Give the preparation type.
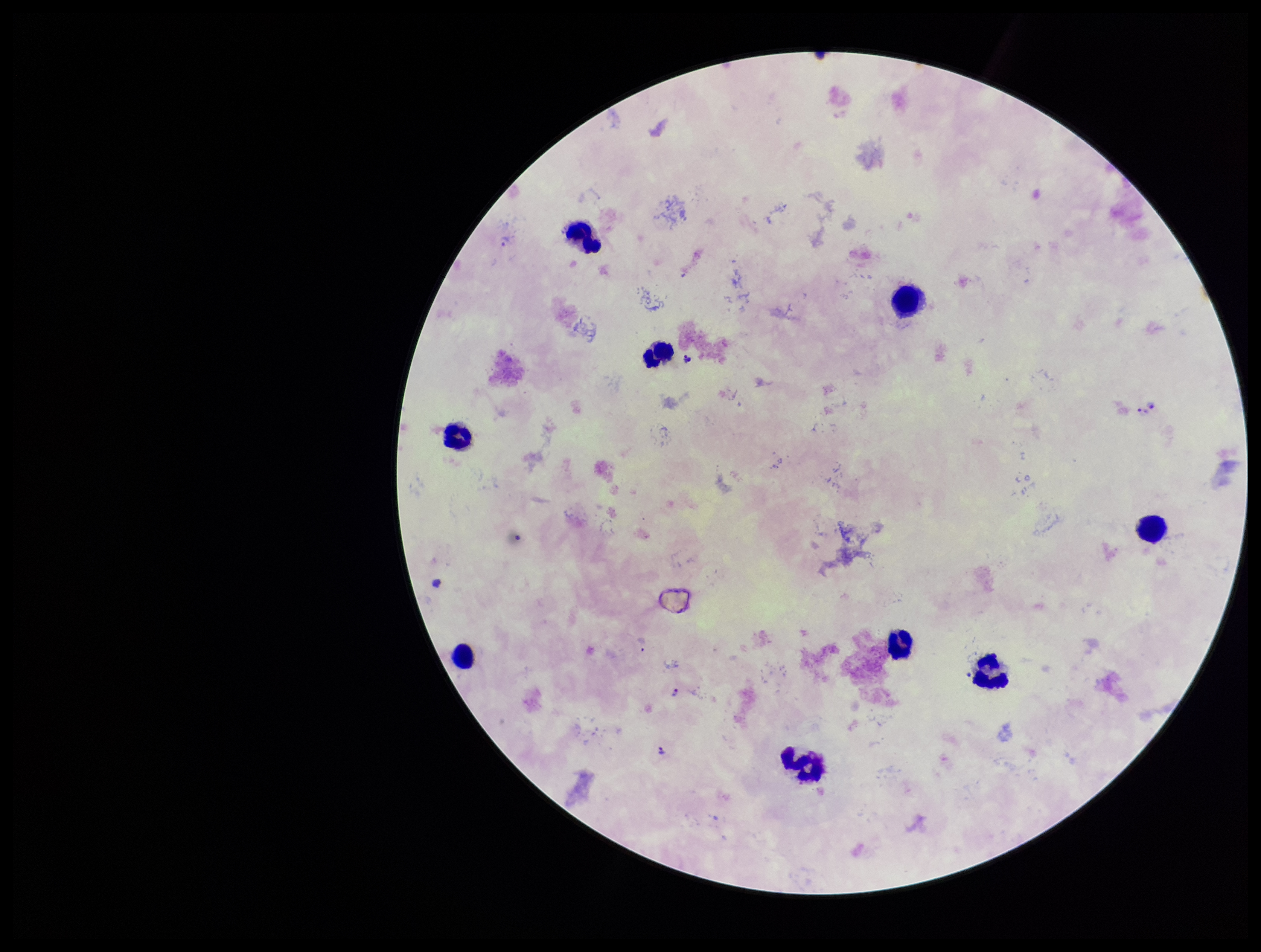
It is a thick blood smear.

Leukocyte count: 9. One field from this slide. Patient malaria status: positive. Smartphone photograph taken through the eyepiece of a microscope. Species reported for this patient: Plasmodium falciparum. Stained with Giemsa. Image is 1261×952 pixels. Plasmodium parasites: detected. Parasite count: 5.